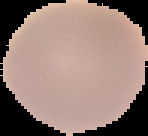 Cell region segmented out of the field of view; the surrounding area is masked to black. Malaria status: uninfected. From a thin blood film. Image is 148×136 pixels.